Report the malaria status of this cell.
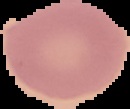
Uninfected.

Image is 130×109 pixels. From a thin blood smear. The area outside the segmented cell region is set to black.